Classify this cell by malaria status.
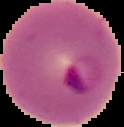
It is parasitized.

Image is 124×127 pixels. The area outside the segmented cell region is set to black. From a thin blood smear.